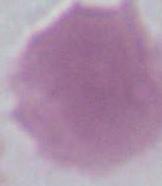
{
  "modality": "micrograph",
  "identification": "erythrocyte",
  "magnification": "1000x"
}